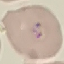

result = malaria parasites identified
image type = cell patch, automatically extracted from a larger field of view and resized to 64 × 64 pixels
capture = smartphone through the microscope eyepiece
preparation = thin blood film
stain = Giemsa